Name the parasite shown.
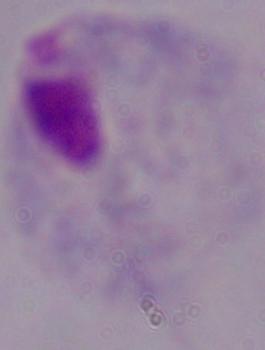

This is a trichomonad.

Summary:
  - Magnification: 1000x
  - Modality: photomicrograph